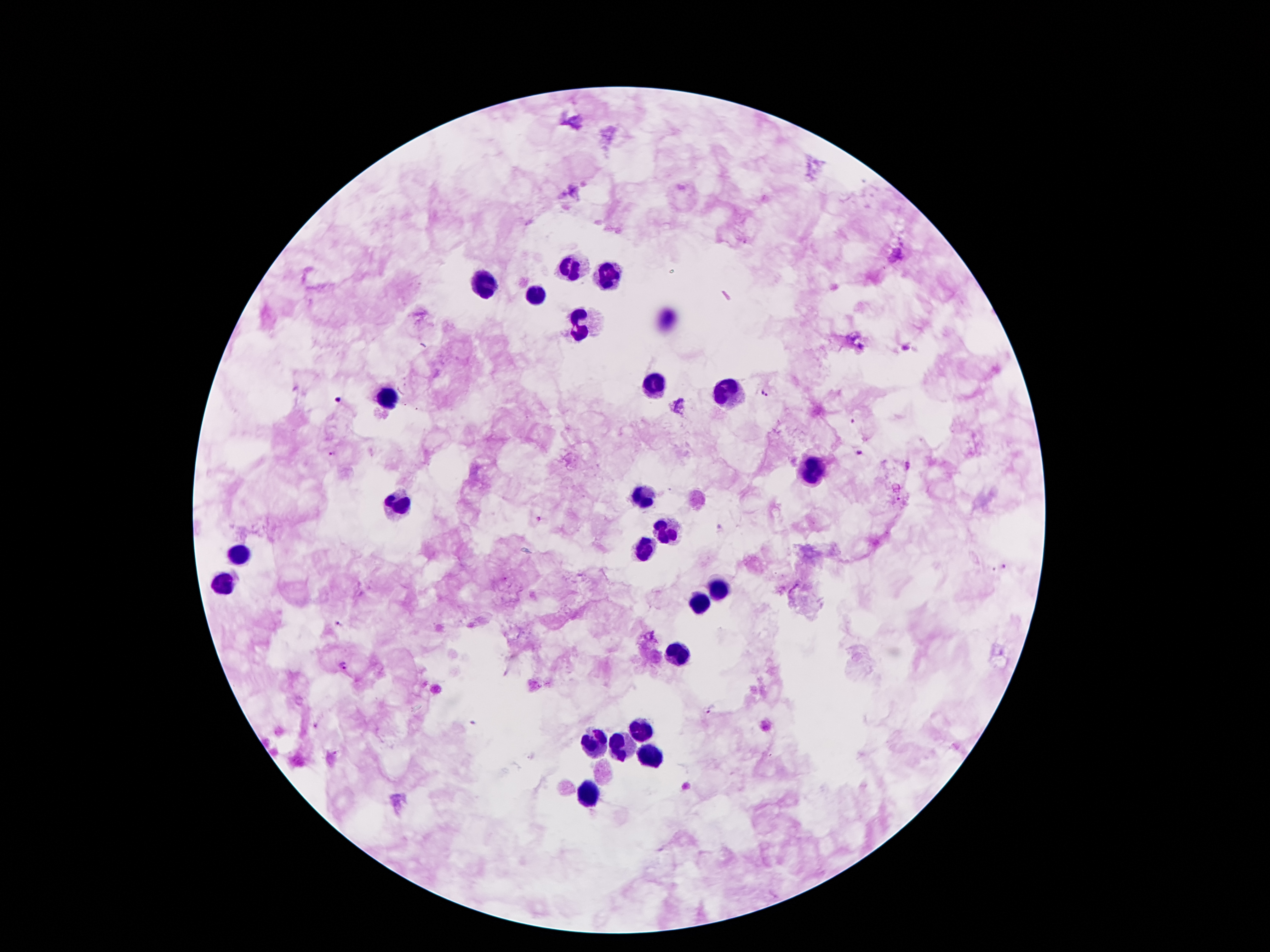
Approximate centers as (x, y) in pixels.
Summary:
  - Leukocyte locations: (572, 264), (606, 278), (484, 283), (538, 294), (581, 324), (656, 385), (729, 392), (384, 394), (811, 473), (643, 496), (399, 507), (668, 530), (645, 546), (239, 549), (223, 580), (718, 589), (699, 603), (677, 653), (640, 730), (597, 741), (622, 746), (654, 757), (588, 796)
  - Malaria parasite locations: (767, 388), (337, 400), (853, 421), (858, 453), (329, 454), (539, 520), (1005, 567), (339, 625), (344, 667), (711, 708)
  - Image size: 1270×952 pixels
  - Capture: smartphone camera through the microscope eyepiece
  - Preparation: thick blood smear
  - Stain: Giemsa
  - Magnification: 100x
  - Patient malaria status: positive for Plasmodium falciparum
  - Field of view: single